State the blood parasite species.
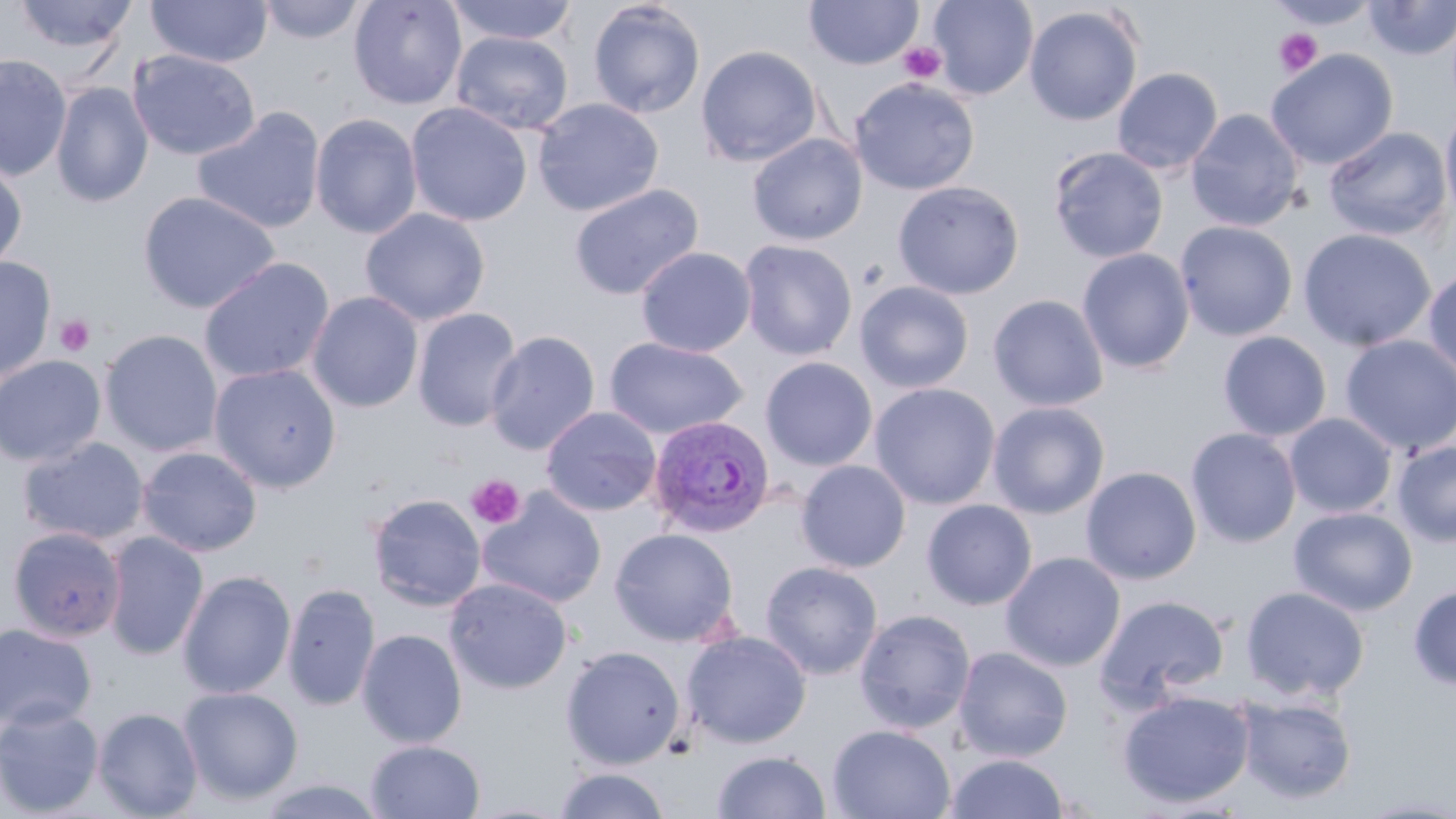

Plasmodium vivax.

image size = 1456×819 pixels
Plasmodium vivax-infected red blood cell locations = approximate bounding boxes as named x1/y1/x2/y2 corners in pixels: (x1=647, y1=414, x2=776, y2=539)
magnification = 1000x
preparation = thin blood smear
uninfected red blood cell locations = approximate bounding boxes as named x1/y1/x2/y2 corners in pixels: (x1=12, y1=0, x2=138, y2=57), (x1=146, y1=0, x2=272, y2=68), (x1=257, y1=0, x2=367, y2=44), (x1=348, y1=0, x2=467, y2=111), (x1=444, y1=0, x2=580, y2=46), (x1=928, y1=0, x2=1038, y2=100), (x1=1362, y1=0, x2=1456, y2=60), (x1=587, y1=1, x2=706, y2=119), (x1=803, y1=1, x2=923, y2=71), (x1=1264, y1=3, x2=1381, y2=31), (x1=1024, y1=5, x2=1144, y2=127), (x1=451, y1=31, x2=574, y2=136), (x1=696, y1=45, x2=823, y2=167), (x1=128, y1=49, x2=260, y2=161), (x1=1265, y1=49, x2=1398, y2=170), (x1=0, y1=55, x2=72, y2=180), (x1=1112, y1=67, x2=1223, y2=175), (x1=849, y1=77, x2=979, y2=195), (x1=51, y1=82, x2=153, y2=208), (x1=532, y1=98, x2=664, y2=217), (x1=406, y1=102, x2=532, y2=227), (x1=1440, y1=104, x2=1456, y2=228), (x1=191, y1=107, x2=326, y2=234), (x1=1186, y1=108, x2=1304, y2=232), (x1=310, y1=113, x2=423, y2=240), (x1=1324, y1=126, x2=1452, y2=241), (x1=747, y1=133, x2=868, y2=246), (x1=1048, y1=146, x2=1169, y2=264), (x1=0, y1=159, x2=27, y2=274), (x1=892, y1=180, x2=1024, y2=300), (x1=568, y1=183, x2=704, y2=300), (x1=137, y1=190, x2=281, y2=315), (x1=360, y1=208, x2=490, y2=326), (x1=1174, y1=221, x2=1299, y2=341), (x1=1297, y1=227, x2=1437, y2=352), (x1=738, y1=239, x2=857, y2=361), (x1=635, y1=246, x2=757, y2=358), (x1=1077, y1=248, x2=1195, y2=374), (x1=198, y1=256, x2=335, y2=384), (x1=0, y1=257, x2=56, y2=385), (x1=1423, y1=263, x2=1456, y2=383), (x1=854, y1=280, x2=974, y2=394), (x1=307, y1=291, x2=424, y2=414), (x1=988, y1=294, x2=1109, y2=412), (x1=412, y1=307, x2=523, y2=432), (x1=100, y1=329, x2=223, y2=459), (x1=485, y1=330, x2=600, y2=456), (x1=1217, y1=331, x2=1332, y2=441), (x1=1339, y1=334, x2=1456, y2=457), (x1=604, y1=337, x2=748, y2=439), (x1=0, y1=355, x2=106, y2=468), (x1=760, y1=356, x2=878, y2=472), (x1=209, y1=364, x2=341, y2=492), (x1=869, y1=382, x2=1001, y2=510), (x1=986, y1=401, x2=1110, y2=519), (x1=540, y1=405, x2=661, y2=517), (x1=1284, y1=412, x2=1398, y2=519), (x1=1185, y1=427, x2=1301, y2=548), (x1=18, y1=436, x2=149, y2=546), (x1=1392, y1=441, x2=1456, y2=547), (x1=137, y1=446, x2=262, y2=557), (x1=796, y1=459, x2=912, y2=573), (x1=1081, y1=466, x2=1202, y2=584), (x1=478, y1=488, x2=607, y2=610), (x1=367, y1=492, x2=486, y2=612), (x1=921, y1=499, x2=1038, y2=610), (x1=1288, y1=506, x2=1418, y2=616), (x1=7, y1=527, x2=126, y2=642), (x1=610, y1=528, x2=739, y2=647), (x1=103, y1=531, x2=208, y2=659), (x1=1000, y1=551, x2=1126, y2=671), (x1=760, y1=561, x2=883, y2=680), (x1=177, y1=569, x2=296, y2=700), (x1=445, y1=577, x2=573, y2=694), (x1=283, y1=582, x2=380, y2=712), (x1=1408, y1=583, x2=1456, y2=691), (x1=1240, y1=586, x2=1370, y2=701), (x1=1095, y1=594, x2=1231, y2=707), (x1=854, y1=608, x2=976, y2=734), (x1=0, y1=623, x2=97, y2=732), (x1=357, y1=628, x2=468, y2=748), (x1=682, y1=630, x2=812, y2=749), (x1=560, y1=645, x2=686, y2=769), (x1=953, y1=646, x2=1073, y2=762), (x1=178, y1=686, x2=303, y2=805), (x1=1117, y1=689, x2=1255, y2=809), (x1=1235, y1=694, x2=1357, y2=804), (x1=0, y1=702, x2=104, y2=817), (x1=93, y1=707, x2=203, y2=819), (x1=827, y1=724, x2=956, y2=819), (x1=365, y1=740, x2=485, y2=818), (x1=711, y1=750, x2=832, y2=818), (x1=944, y1=753, x2=1070, y2=818), (x1=552, y1=767, x2=672, y2=819), (x1=255, y1=776, x2=389, y2=819), (x1=1353, y1=796, x2=1456, y2=818)
platelet locations = approximate bounding boxes as named x1/y1/x2/y2 corners in pixels: (x1=1273, y1=28, x2=1323, y2=78), (x1=897, y1=42, x2=946, y2=84), (x1=55, y1=314, x2=95, y2=357), (x1=465, y1=474, x2=525, y2=529)
modality = optical microscopy
stain = May-Grünwald-Giemsa
field of view = one of a larger specimen